Classify this cell by malaria status.
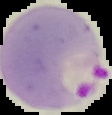
It is parasitized.

image size = 112×115 pixels
preparation = thin blood film
image type = segmented cell region on a black background